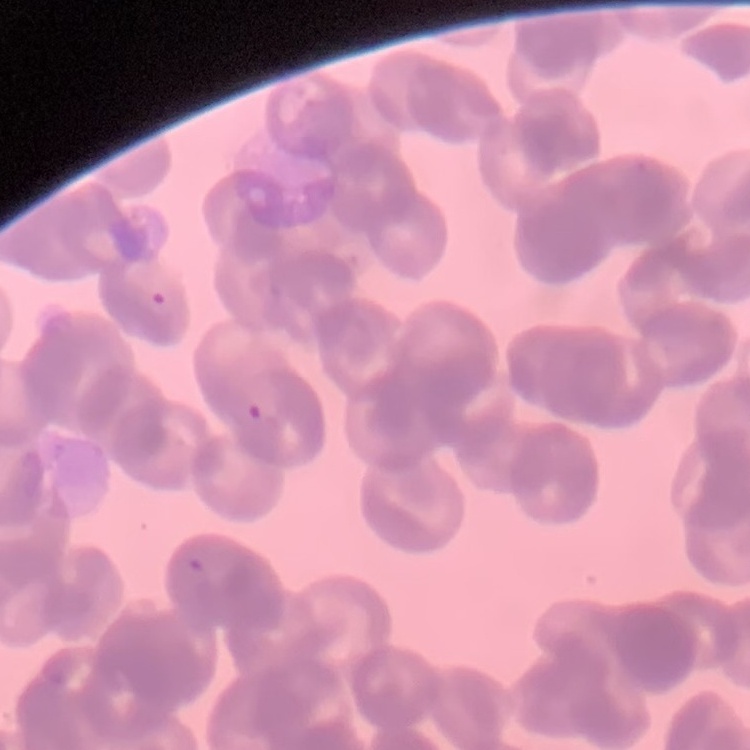
The erythrocytes exhibit rouleaux formation. Thin peripheral smear. One tile cut from a larger photomicrograph. Stained with either Field's or Giemsa.